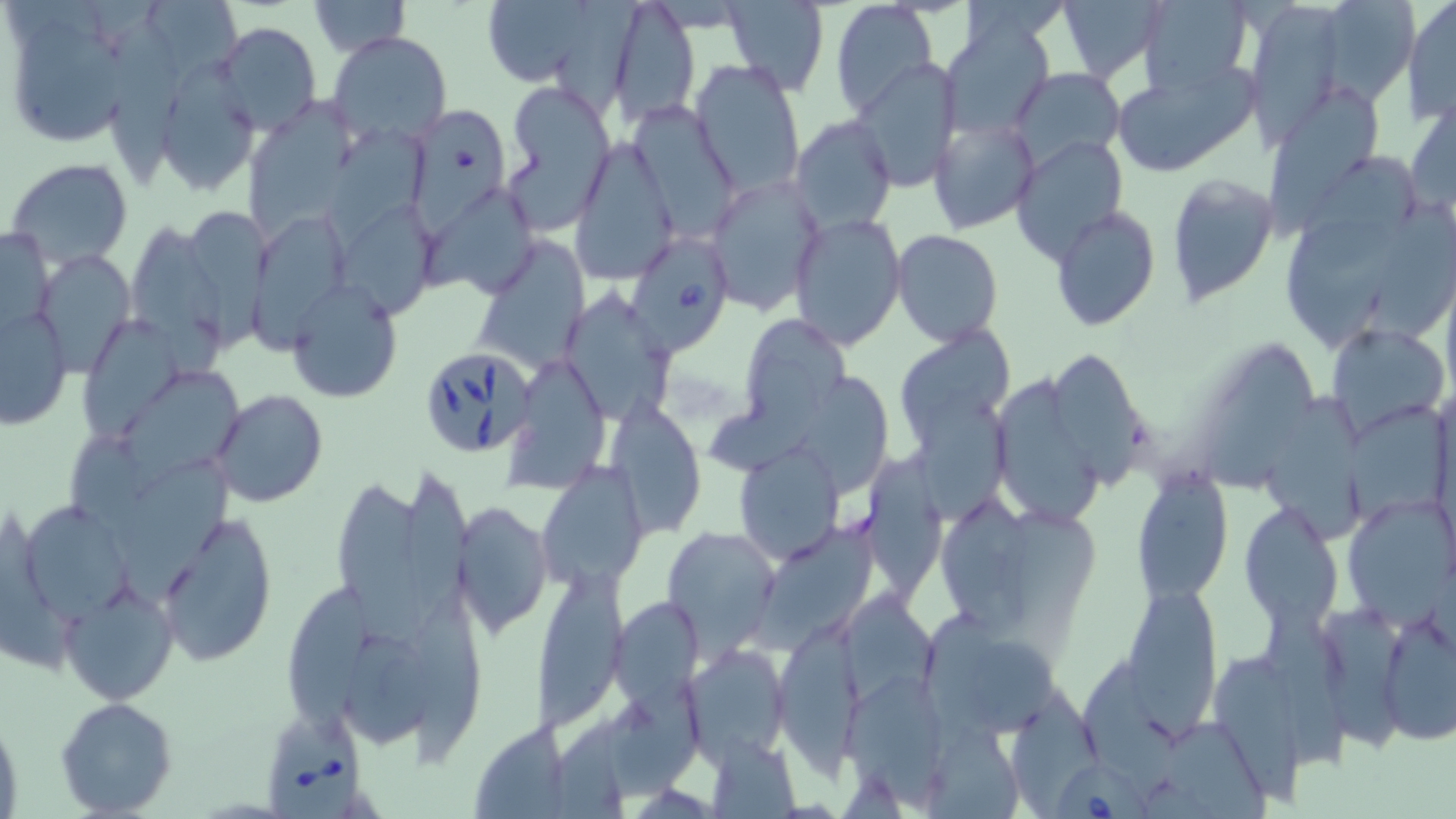

Approximate bounding boxes as (x1, y1, x2, y2) in pixels. Babesia divergens-infected red blood cell locations: (630, 230, 734, 351), (418, 346, 536, 460), (264, 710, 368, 819), (1056, 764, 1156, 819). Uninfected red blood cell locations: (477, 0, 614, 91), (607, 0, 701, 126), (1058, 0, 1166, 84), (1137, 0, 1255, 95), (1310, 0, 1421, 109), (309, 1, 409, 56), (721, 1, 830, 96), (1402, 1, 1455, 124), (830, 2, 936, 122), (148, 3, 249, 73), (1244, 3, 1345, 145), (937, 15, 1058, 144), (111, 19, 174, 184), (213, 22, 321, 137), (20, 28, 134, 145), (329, 31, 453, 148), (850, 58, 962, 192), (690, 59, 805, 198), (1112, 60, 1260, 177), (1010, 68, 1126, 170), (155, 69, 257, 197), (502, 80, 616, 231), (1270, 93, 1377, 239), (249, 95, 355, 242), (1406, 95, 1455, 216), (629, 102, 738, 235), (413, 108, 506, 237), (790, 115, 896, 233), (929, 118, 1039, 233), (325, 129, 428, 252), (1011, 133, 1129, 263), (572, 135, 678, 284), (1298, 152, 1419, 251), (5, 157, 135, 272), (704, 172, 825, 314), (1167, 175, 1281, 307), (424, 194, 538, 298), (1374, 201, 1456, 336), (340, 202, 435, 313), (1050, 206, 1160, 331), (186, 207, 273, 354), (789, 211, 906, 350), (254, 215, 350, 360), (1285, 220, 1395, 354), (0, 223, 55, 333), (129, 225, 227, 376), (893, 230, 1004, 347), (472, 237, 591, 378), (37, 250, 132, 375), (287, 283, 403, 403), (566, 283, 681, 416), (1, 303, 73, 427), (742, 313, 850, 427), (72, 317, 197, 446), (1327, 323, 1450, 439), (902, 327, 1014, 447), (1207, 343, 1319, 492), (1056, 354, 1139, 490), (507, 357, 609, 488), (126, 367, 240, 494), (801, 374, 892, 500), (995, 379, 1098, 524), (1265, 388, 1367, 541), (211, 389, 329, 507), (914, 391, 1010, 525), (1350, 398, 1450, 523), (607, 400, 708, 536), (706, 408, 827, 476), (68, 437, 157, 527), (732, 442, 847, 565), (116, 454, 231, 609), (863, 457, 947, 607), (532, 465, 646, 593), (402, 471, 471, 638), (1130, 471, 1235, 602), (339, 482, 424, 647), (941, 495, 1023, 628), (1342, 495, 1454, 624), (18, 499, 134, 618), (453, 501, 554, 640), (1240, 502, 1342, 627), (155, 511, 280, 668), (664, 526, 781, 653), (755, 528, 876, 652), (539, 567, 628, 731), (60, 581, 178, 706), (288, 584, 367, 745), (846, 587, 941, 707), (1124, 587, 1221, 726), (411, 595, 483, 766), (613, 597, 703, 710), (925, 604, 1001, 733), (1326, 605, 1404, 760), (1376, 611, 1456, 745), (782, 621, 862, 782), (1259, 622, 1350, 775), (340, 633, 435, 750), (965, 637, 1059, 736), (685, 644, 790, 764), (1214, 654, 1303, 810), (1083, 665, 1175, 794), (848, 677, 948, 807), (610, 678, 703, 801), (1014, 690, 1098, 819), (55, 697, 179, 818), (0, 706, 24, 815), (553, 712, 621, 819), (469, 721, 572, 817), (1169, 724, 1268, 819), (925, 727, 1023, 817), (704, 736, 799, 816). Slide-level diagnosis: Babesia divergens. Image is 1456×819 pixels. Light microscopy. Thin blood film. One field of a larger specimen. Captured at 1000x magnification. May-Grünwald-Giemsa stain.